Classify this cell by malaria status.
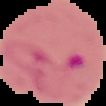
Parasitized.

image type = segmented cell region with the area outside set to black
image size = 106×106 pixels
preparation = thin blood film